Report the malaria status of this cell.
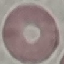

It is uninfected.

Summary:
  - Preparation: thin blood smear
  - Stain: Giemsa
  - Capture: smartphone through the microscope eyepiece
  - Image type: cell patch, automatically extracted from a larger field of view and resized to 64 × 64 pixels